Describe the morphology of the red blood cells.
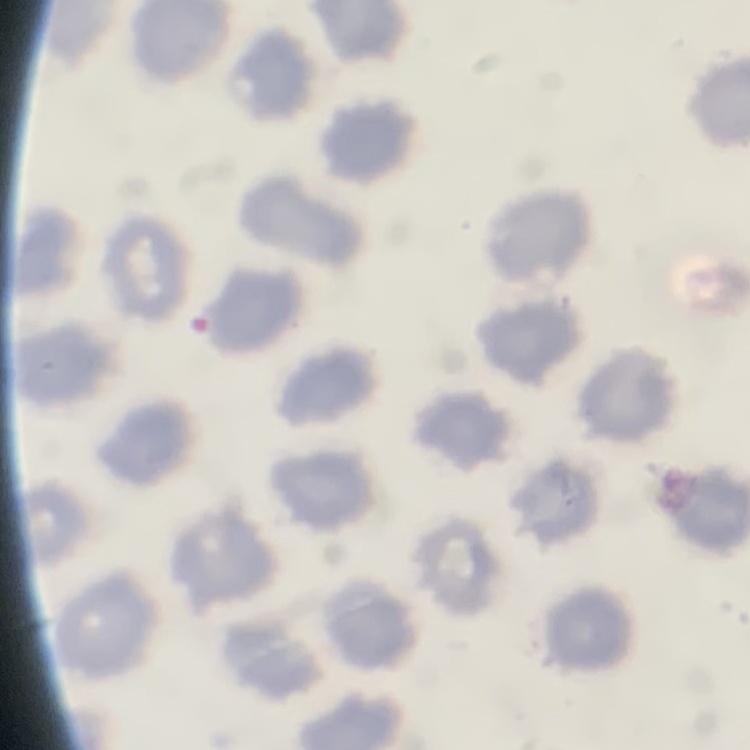

No rouleaux formation.

{
  "preparation": "thin peripheral smear",
  "image_type": "square crop of a larger photomicrograph",
  "stain": "Field's or Giemsa"
}